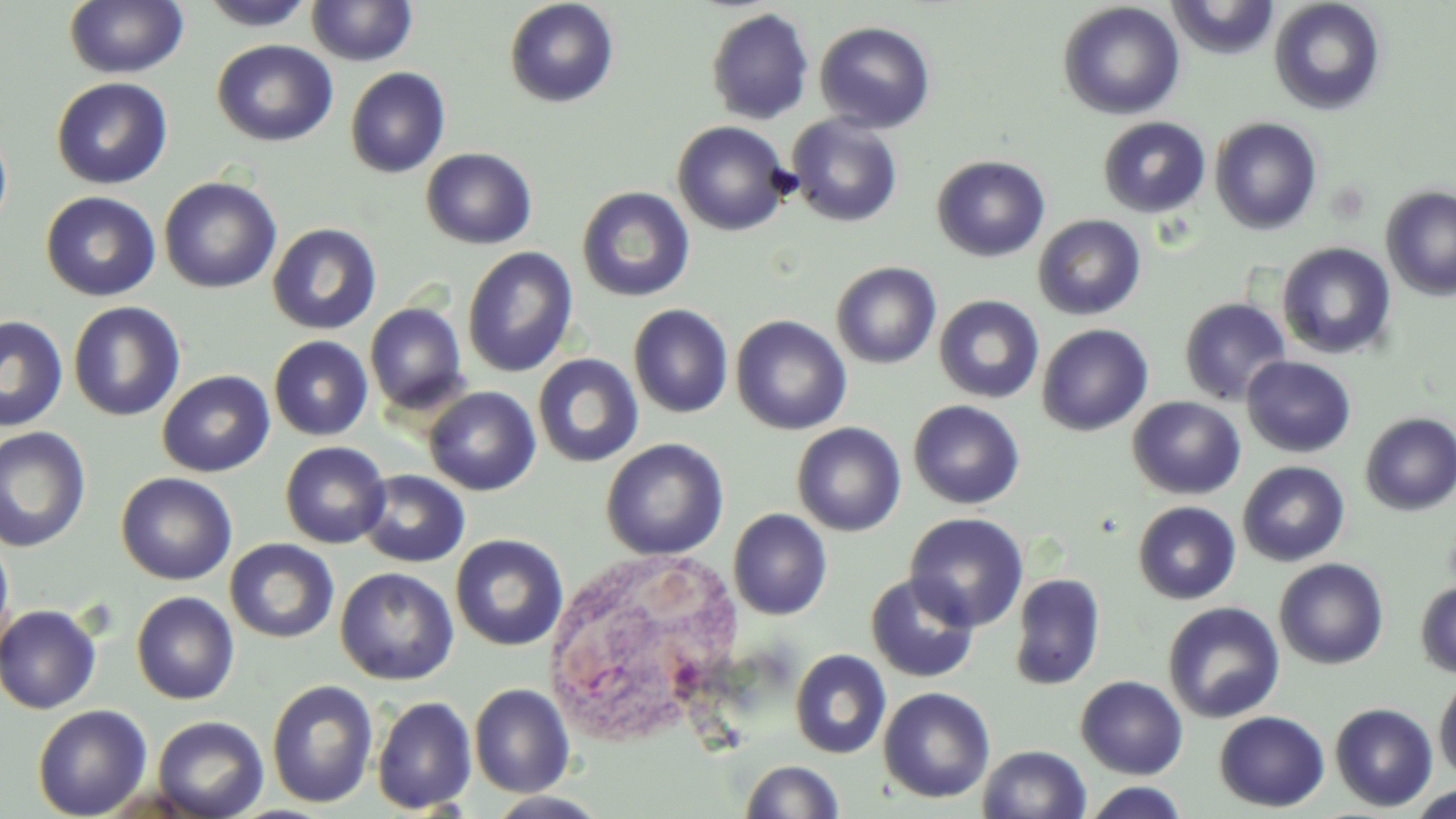
slide-level diagnosis = negative for blood parasites
modality = light microscopy
uninfected red blood cell locations = approximate bounding boxes as (x1,y1)-(x2,y2) corner pairs in pixels: (199,0)-(317,30), (306,0)-(418,66), (504,0)-(619,108), (1167,0)-(1280,59), (1268,0)-(1386,115), (64,1)-(189,79), (1057,2)-(1185,120), (706,7)-(815,125), (814,20)-(936,133), (212,39)-(337,147), (345,67)-(450,178), (51,77)-(172,189), (786,115)-(903,228), (1098,116)-(1210,218), (1209,116)-(1322,234), (0,119)-(13,236), (672,121)-(792,236), (420,147)-(537,250), (931,155)-(1050,262), (158,176)-(282,294), (576,186)-(695,302), (1381,186)-(1456,301), (41,191)-(160,301), (1032,214)-(1146,320), (268,223)-(382,335), (1277,242)-(1396,359), (462,247)-(579,378), (830,262)-(942,368), (933,295)-(1045,404), (1179,297)-(1291,406), (67,301)-(185,421), (364,302)-(469,416), (628,303)-(733,418), (0,315)-(68,431), (731,315)-(851,434), (1037,324)-(1154,436), (268,335)-(373,441), (532,353)-(644,468), (1241,356)-(1357,457), (157,370)-(275,477), (424,386)-(541,496), (1128,396)-(1246,500), (908,400)-(1025,509), (1360,412)-(1455,516), (791,422)-(906,536), (0,426)-(92,552), (601,438)-(728,560), (280,441)-(391,549), (1237,460)-(1350,566), (356,470)-(470,568), (116,472)-(237,585), (1133,501)-(1241,604), (728,508)-(832,620), (904,512)-(1028,631), (0,532)-(14,659), (450,534)-(569,650), (225,538)-(339,643), (1274,558)-(1389,670), (335,567)-(459,685), (1010,572)-(1105,690), (865,573)-(980,683), (1415,580)-(1456,678), (131,591)-(239,704), (1162,602)-(1285,723), (0,604)-(102,714), (789,649)-(892,759), (1434,673)-(1456,782), (1075,675)-(1189,779), (266,679)-(379,808), (469,683)-(575,797), (878,686)-(995,803), (371,696)-(477,814), (1330,703)-(1438,811), (32,704)-(153,819), (1214,711)-(1330,811), (152,715)-(269,818), (978,745)-(1091,819), (739,759)-(845,818), (1082,782)-(1190,818), (1407,784)-(1456,817), (484,791)-(608,819)
image size = 1456×819 pixels
magnification = 1000x
field of view = single
preparation = thin blood smear
stain = May-Grünwald-Giemsa
white blood cell locations = approximate bounding boxes as (x1,y1)-(x2,y2) corner pairs in pixels: (546,548)-(741,743)